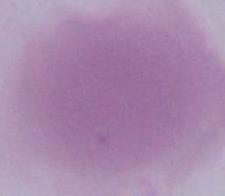
1000x magnification. Micrograph. A red blood cell is shown.